Point out each leukocyte.
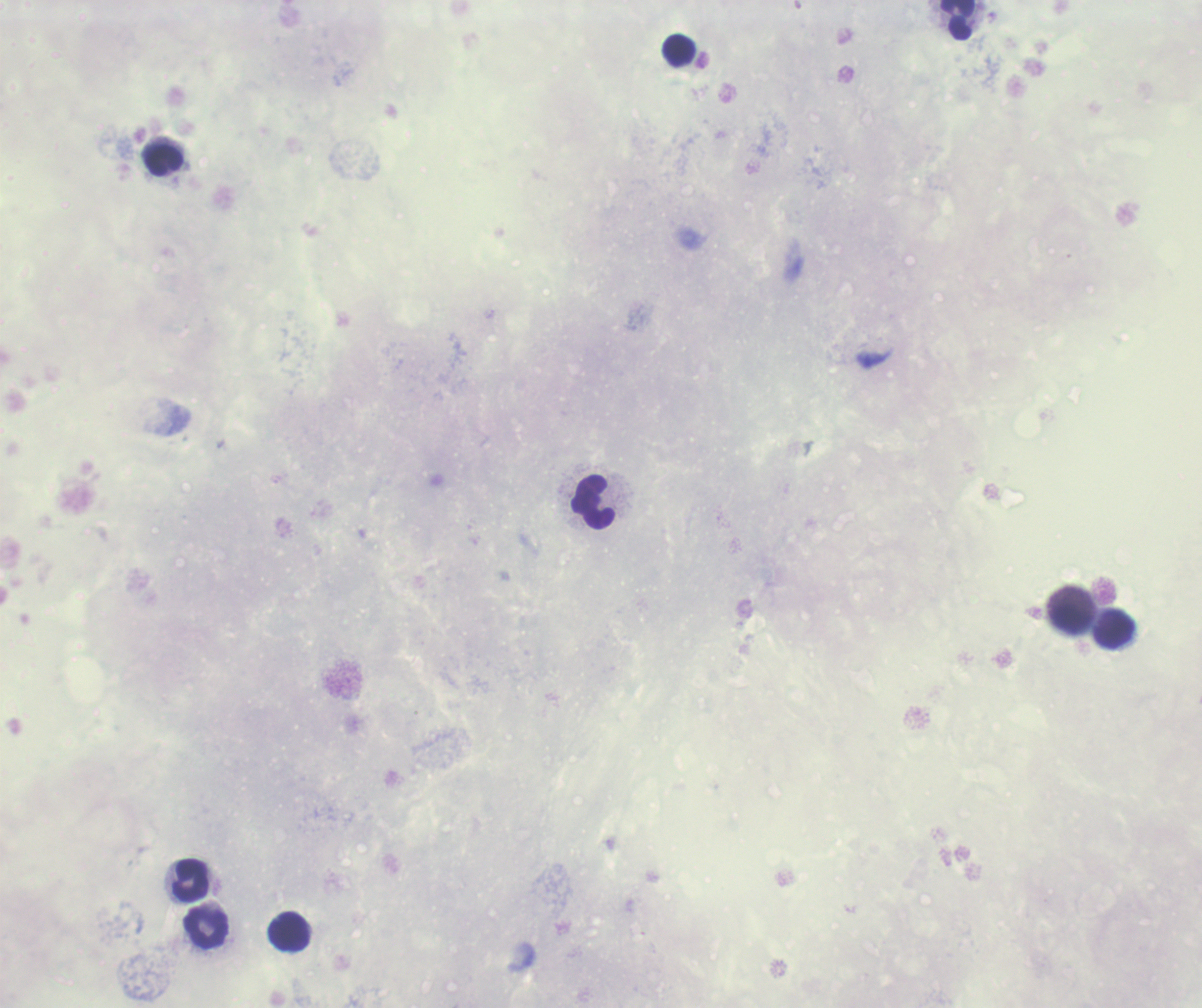
Approximate centers as {x, y} in pixels.
Leukocytes: {957, 19}, {679, 50}, {165, 159}, {594, 501}, {1071, 619}, {1115, 629}, {192, 880}, {206, 928}, {290, 932}.

Summary:
  - Field of view: one from this slide
  - Magnification: 100x
  - Background quality: poor
  - Result: negative for malaria parasites
  - Stain: Romanowsky
  - Image size: 1202×1008 pixels
  - Context: previously used in a real diagnosis
  - Coloration quality: bad
  - Preparation: thick blood smear